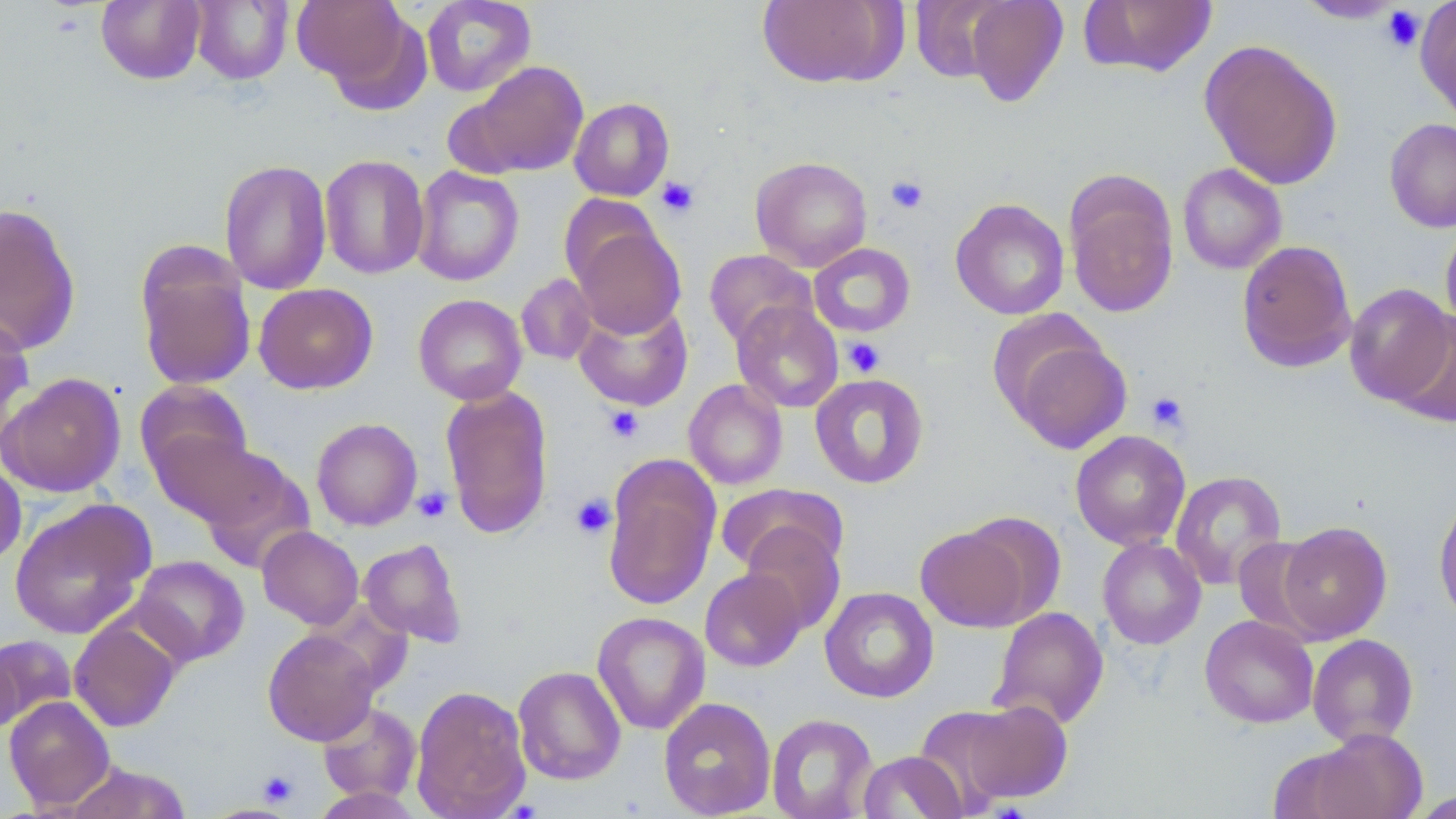
{
  "slide_level_diagnosis": "no evidence of blood parasites",
  "stain": "May-Grünwald-Giemsa",
  "image_size": "1456×819 pixels",
  "field_of_view": "single",
  "uninfected_red_blood_cell_locations": "approximate bounding boxes as (x1,y1)-(x2,y2) corner pairs in pixels: (96,0)-(206,85), (190,0)-(293,85), (291,0)-(418,98), (421,0)-(537,97), (757,0)-(903,88), (963,0)-(1069,108), (1079,0)-(1218,78), (1294,0)-(1407,24), (909,1)-(1013,84), (1415,1)-(1456,121), (1199,38)-(1344,190), (464,61)-(589,177), (569,97)-(674,201), (1384,118)-(1456,233), (319,154)-(430,280), (751,156)-(873,271), (219,158)-(333,295), (1177,163)-(1287,274), (411,165)-(525,286), (1064,172)-(1179,318), (562,193)-(662,288), (950,198)-(1070,320), (0,203)-(82,354), (569,221)-(686,339), (1440,223)-(1456,337), (1236,240)-(1357,373), (808,243)-(916,337), (135,245)-(257,392), (704,249)-(816,349), (516,274)-(597,365), (253,283)-(378,394), (1344,283)-(1454,408), (413,294)-(527,405), (731,300)-(844,413), (574,301)-(693,412), (1388,308)-(1456,429), (0,309)-(35,446), (999,329)-(1133,457), (1,372)-(126,497), (809,373)-(929,489), (683,378)-(788,490), (135,380)-(253,485), (440,385)-(554,539), (311,417)-(422,531), (1070,430)-(1191,551), (150,431)-(272,527), (195,446)-(314,572), (603,457)-(721,611), (0,458)-(26,568), (1170,470)-(1287,589), (716,483)-(848,577), (1434,493)-(1456,625), (9,499)-(154,640), (1277,521)-(1392,643), (740,523)-(846,634), (916,524)-(1033,632), (257,525)-(364,630), (1232,536)-(1329,637), (358,537)-(468,648), (1097,537)-(1206,649), (131,555)-(249,665), (700,568)-(806,672), (820,586)-(938,703), (990,606)-(1109,729), (591,611)-(710,734), (1200,614)-(1319,728), (69,619)-(181,732), (262,628)-(380,745), (1307,633)-(1419,747), (0,634)-(78,731), (0,644)-(20,736), (513,665)-(626,786), (410,685)-(531,819), (4,695)-(115,811), (658,696)-(776,818), (962,699)-(1074,803), (317,702)-(422,803), (913,706)-(1022,816), (766,713)-(878,819), (1301,730)-(1429,818), (857,751)-(966,818), (66,761)-(191,818), (308,785)-(425,818), (1408,789)-(1456,817)",
  "platelet_locations": "approximate bounding boxes as (x1,y1)-(x2,y2) corner pairs in pixels: (1381,4)-(1425,53), (885,175)-(929,214), (656,176)-(699,217), (842,337)-(885,377), (1146,391)-(1189,433), (604,405)-(644,443), (413,486)-(452,523), (571,492)-(616,539), (259,770)-(299,806)",
  "magnification": "1000x",
  "modality": "light microscopy",
  "preparation": "thin blood film"
}